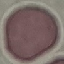 Result: negative for malaria parasites. Thin smear of blood. Cell patch, automatically extracted from a larger field of view and resized to 64 × 64 pixels. Photographed with a smartphone camera at the microscope eyepiece. Giemsa stain.